Comment on the morphology of the erythrocytes.
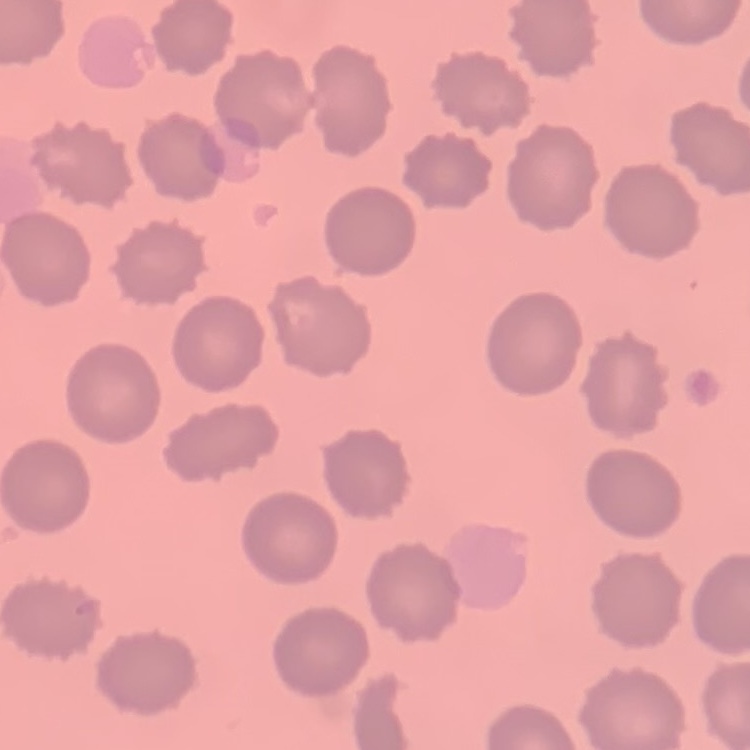
They show no rouleaux formation.

One tile cut from a larger photomicrograph. Thin blood film. Field's or Giemsa stain.